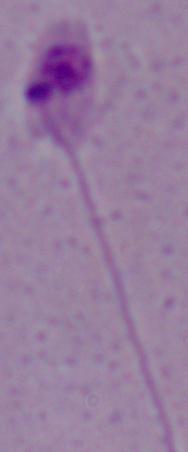
{
  "modality": "micrograph",
  "identification": "Leishmania",
  "magnification": "1000x"
}